Assess this cell for malaria.
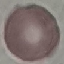
Uninfected.

{
  "capture": "smartphone camera at the microscope eyepiece",
  "stain": "Giemsa",
  "preparation": "thin blood film",
  "image_type": "automatically extracted cell patch, resized to 64 × 64 pixels"
}